Describe the morphology of the erythrocytes.
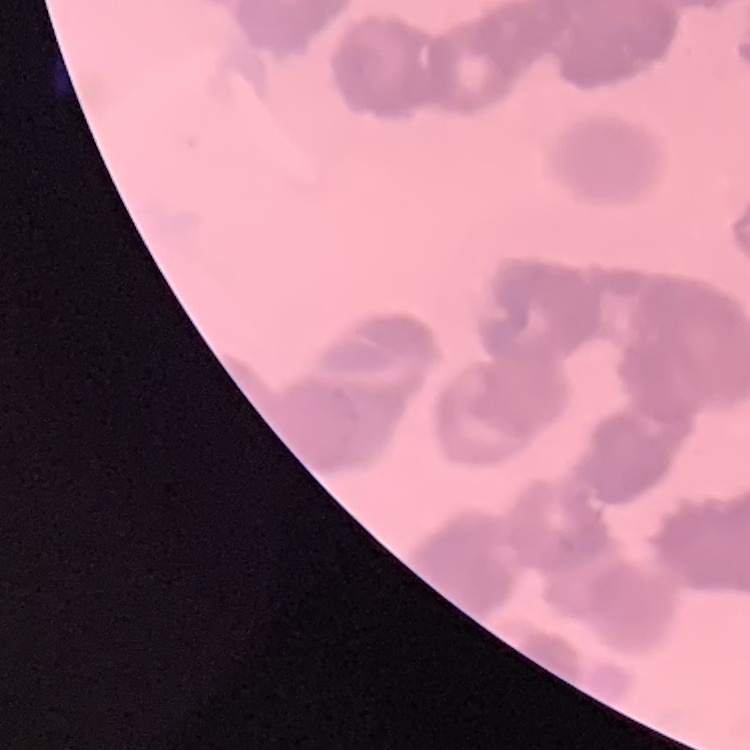
They show rouleaux formation.

Thin blood smear. Field's or Giemsa stain. One tile cut from a larger photomicrograph.